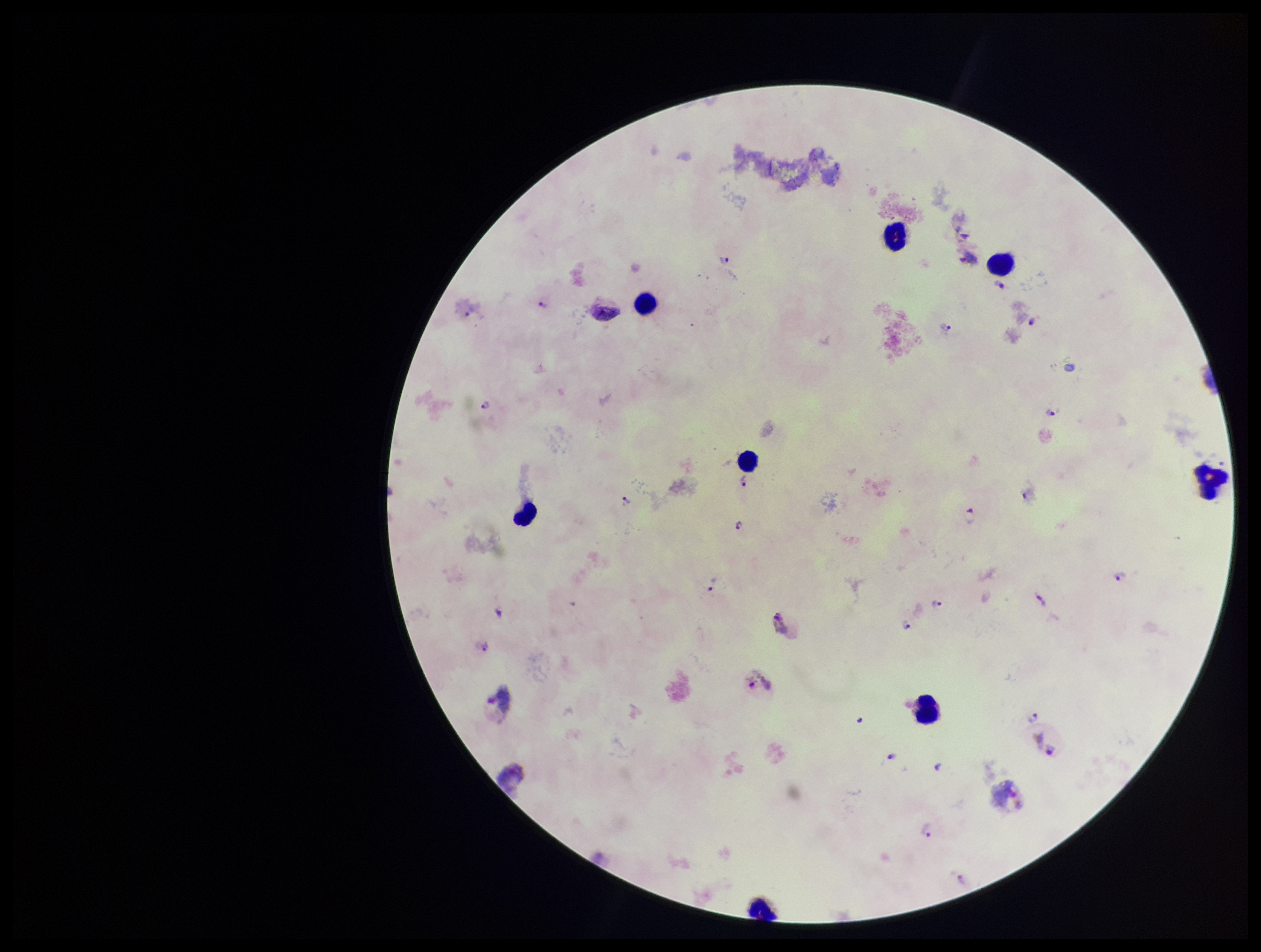

Photographed through the microscope eyepiece with a smartphone camera. Plasmodium parasites: identified. Preparation: thick smear. Image is 1261×952 pixels. Patient malaria status: positive. Leukocyte count: 8. Stained with Giemsa. Parasite count: 26. Species reported for this patient: Plasmodium vivax. Single field of view.